Assess this cell for malaria.
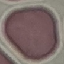
It is uninfected.

Summary:
  - Capture: smartphone camera at the microscope eyepiece
  - Image type: cell patch, automatically extracted from a larger field of view and resized to 64 × 64 pixels
  - Preparation: thin smear
  - Stain: Giemsa